Assess the morphology of the erythrocytes.
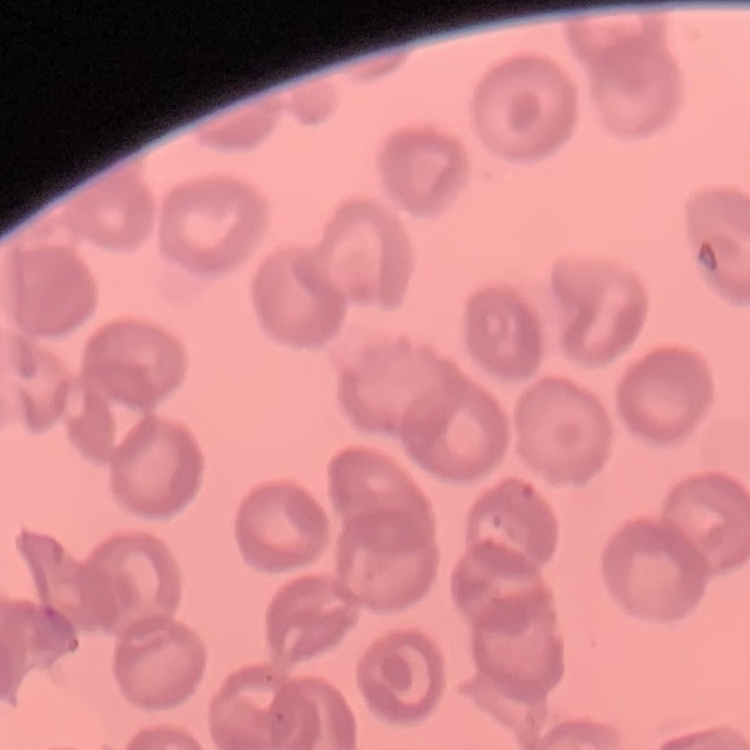
No rouleaux formation.

image_type: one tile cut from a larger photomicrograph
preparation: thin peripheral smear
stain: Field's or Giemsa